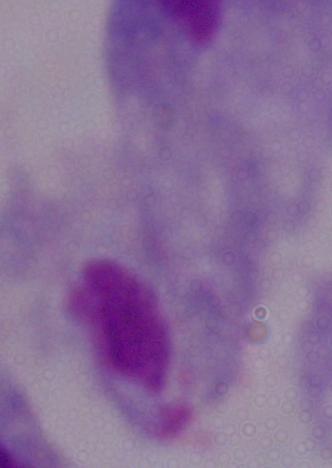
Summary:
  - Modality: micrograph
  - Identification: trichomonad
  - Magnification: 1000x